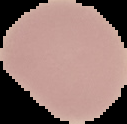
The area outside the segmented cell region is set to black. Image is 127×124 pixels. From a thin blood film. Result: negative for Plasmodium parasites.